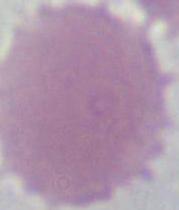

Micrograph. 1000x magnification. An erythrocyte is seen.